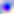

magnification: 400x
identification: Toxoplasma gondii
modality: micrograph